State which parasite is depicted.
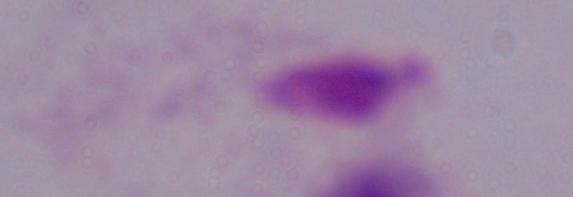
This is a trichomonad.

Summary:
  - Modality: micrograph
  - Magnification: 1000x